Give the extent of all Plasmodium vivax-infected red blood cells.
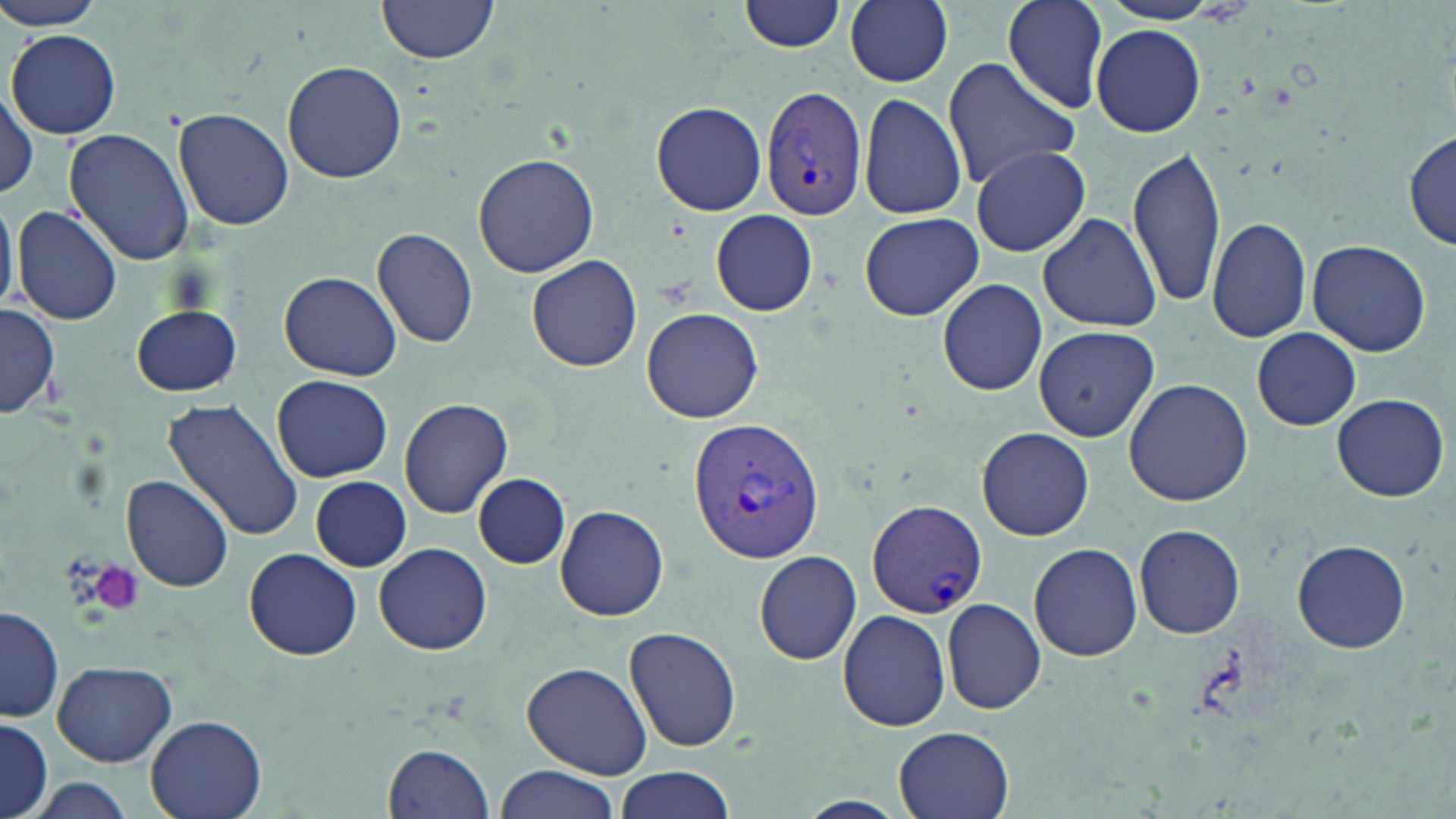
Approximate bounding boxes as (x1, y1, x2, y2) in pixels.
Plasmodium vivax-infected red blood cells: (760, 85, 867, 220), (685, 418, 824, 562), (869, 501, 987, 618).

slide-level diagnosis = Plasmodium vivax
field of view = one of a larger specimen
magnification = 1000x
stain = May-Grünwald-Giemsa
modality = optical microscopy
platelet locations = approximate bounding boxes as (x1, y1, x2, y2) in pixels: (88, 561, 145, 614)
image size = 1456×819 pixels
preparation = thin blood smear
uninfected red blood cell locations = approximate bounding boxes as (x1, y1, x2, y2) in pixels: (0, 0, 113, 31), (374, 0, 501, 66), (739, 0, 847, 53), (1002, 0, 1110, 112), (1093, 0, 1233, 26), (845, 1, 953, 87), (1091, 25, 1206, 137), (7, 28, 123, 140), (941, 57, 1081, 191), (282, 60, 406, 183), (0, 85, 39, 199), (857, 93, 968, 221), (651, 101, 767, 216), (172, 106, 294, 231), (63, 129, 193, 266), (1405, 130, 1455, 252), (1129, 144, 1228, 309), (969, 146, 1091, 257), (473, 152, 599, 278), (0, 190, 17, 315), (12, 205, 122, 326), (710, 211, 818, 316), (1037, 211, 1163, 332), (858, 212, 984, 321), (1207, 214, 1312, 343), (372, 227, 480, 349), (1306, 240, 1430, 356), (527, 254, 643, 373), (279, 271, 402, 381), (938, 278, 1047, 396), (132, 304, 243, 396), (0, 305, 61, 419), (641, 308, 764, 423), (1032, 325, 1161, 442), (1252, 328, 1360, 430), (271, 375, 393, 482), (1123, 378, 1253, 506), (1331, 391, 1449, 501), (162, 397, 304, 545), (399, 397, 515, 518), (977, 427, 1093, 540), (120, 473, 235, 593), (473, 473, 569, 567), (306, 477, 411, 570), (555, 504, 669, 621), (1135, 523, 1244, 639), (1291, 538, 1412, 654), (374, 542, 493, 655), (1029, 542, 1142, 661), (244, 548, 364, 661), (754, 549, 861, 665), (942, 598, 1046, 714), (1, 604, 63, 724), (837, 609, 952, 732), (625, 626, 741, 752), (51, 659, 177, 767), (521, 661, 655, 781), (145, 713, 268, 819), (0, 720, 54, 818), (891, 724, 1018, 819), (383, 743, 495, 819), (494, 763, 621, 819), (613, 766, 734, 819), (19, 778, 142, 819)